Classify this cell by malaria status.
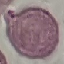
It is uninfected.

image type = cell patch, automatically extracted from a larger field of view and resized to 64 × 64 pixels
preparation = thin blood film
stain = Giemsa
capture = smartphone through the microscope eyepiece